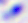
magnification: 400x
modality: photomicrograph
identification: Toxoplasma gondii